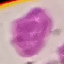
Malaria status: uninfected. Thin smear of blood. Acquired by smartphone through the microscope eyepiece. Automatically extracted cell patch, resized to 64 × 64 pixels. Giemsa-stained preparation.